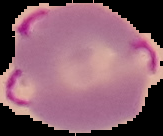

image_type: segmented cell region with the area outside set to black
preparation: thin blood film
image_size: 163×136 pixels
malaria_status: parasitized